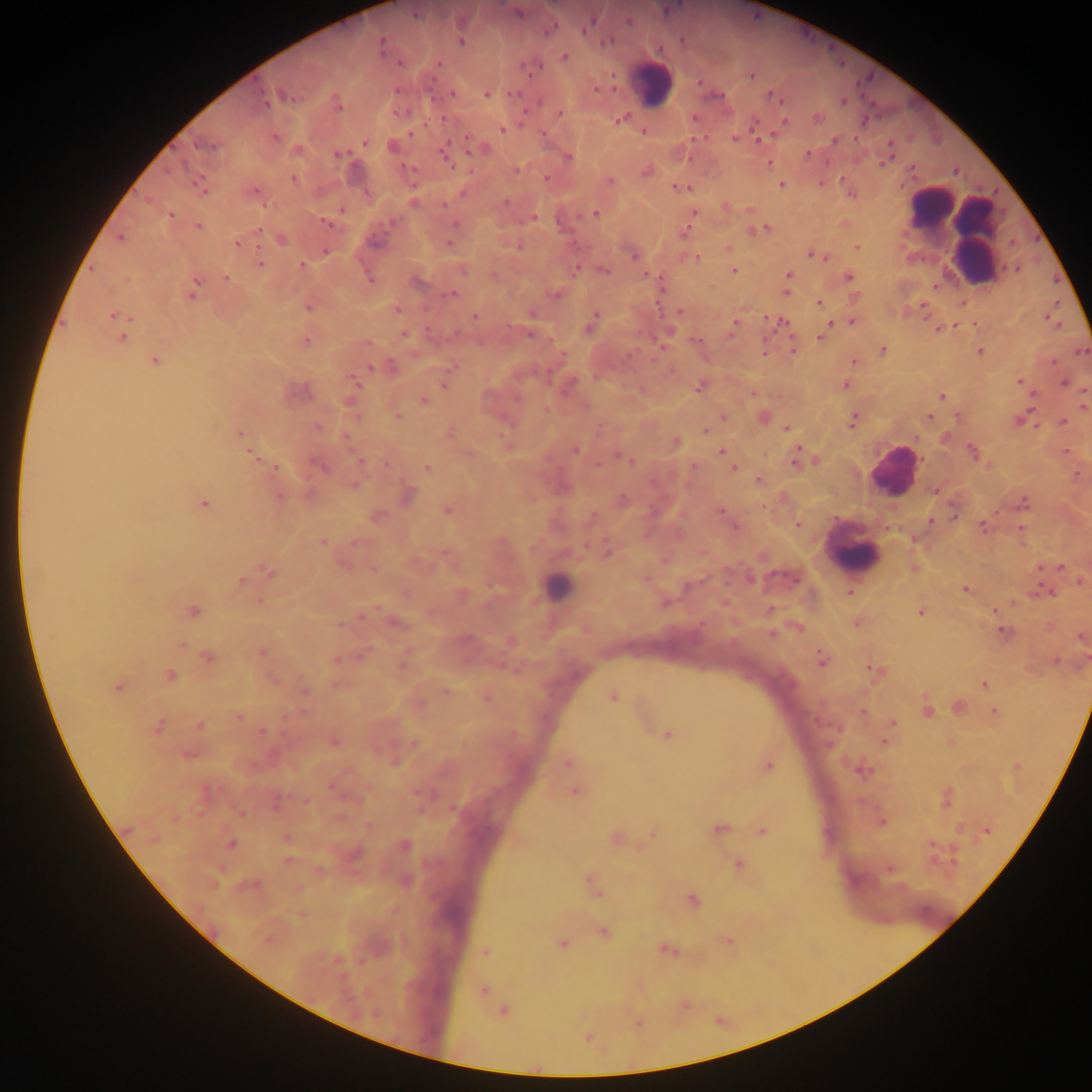 Approximate centers as [x, y] in pixels. Malaria parasite locations: [518, 13], [416, 15], [590, 23], [551, 29], [462, 41], [607, 42], [381, 45], [564, 56], [398, 62], [438, 64], [751, 76], [452, 94], [486, 95], [771, 96], [291, 97], [265, 101], [843, 102], [338, 105], [560, 114], [817, 117], [620, 119], [784, 122], [502, 129], [411, 133], [543, 134], [275, 137], [734, 137], [467, 138], [835, 141], [365, 142], [204, 146], [392, 146], [443, 151], [340, 155], [807, 155], [568, 157], [769, 163], [883, 163], [517, 170], [647, 171], [294, 178], [547, 178], [610, 181], [781, 185], [678, 187], [201, 188], [255, 191], [463, 193], [506, 202], [444, 205], [342, 210], [595, 213], [694, 213], [170, 215], [534, 218], [326, 223], [454, 224], [198, 226], [258, 229], [765, 229], [121, 239], [281, 239], [237, 244], [448, 244], [856, 246], [326, 251], [633, 256], [814, 256], [697, 258], [260, 263], [302, 265], [575, 269], [463, 270], [734, 271], [604, 272], [789, 274], [849, 278], [225, 279], [369, 279], [195, 285], [786, 292], [452, 294], [553, 294], [192, 295], [818, 303], [308, 307], [397, 309], [679, 312], [112, 315], [474, 315], [595, 315], [593, 321], [782, 322], [852, 322], [735, 324], [590, 328], [938, 328], [531, 334], [403, 335], [122, 337], [822, 337], [306, 342], [793, 349], [883, 351], [980, 352], [155, 362], [852, 362], [392, 367], [371, 368], [353, 380], [1019, 382], [1064, 383], [845, 385], [444, 386], [700, 387], [943, 396], [517, 398], [424, 402], [398, 416], [724, 416], [764, 417], [929, 417], [852, 420], [1063, 422], [318, 427], [787, 428], [705, 430], [239, 434], [347, 438], [676, 443], [575, 450], [722, 451], [974, 452], [618, 455], [254, 456], [624, 458], [796, 459], [360, 460], [598, 465], [693, 466], [320, 467], [276, 468], [427, 468], [733, 468], [1077, 474], [758, 479], [354, 485], [935, 491], [279, 497], [623, 501], [1024, 501], [203, 504], [447, 511], [719, 512], [377, 517], [797, 524], [983, 526], [736, 527], [323, 541], [355, 543], [608, 552], [1060, 567], [373, 569], [270, 573], [646, 580], [240, 582], [965, 589], [850, 592], [995, 611], [193, 612], [921, 612], [1004, 632], [772, 634], [1082, 637], [182, 645], [262, 653], [207, 657], [821, 659], [337, 660], [876, 670], [170, 676], [273, 681], [984, 684], [117, 688], [304, 688], [446, 692], [612, 697], [487, 698], [960, 708], [928, 711], [994, 711], [863, 712], [238, 717], [893, 722], [199, 725], [159, 726], [262, 732], [668, 735], [334, 742], [885, 742], [567, 763], [768, 766], [863, 772], [576, 791], [947, 798], [306, 801], [241, 814], [719, 830], [986, 830], [763, 831], [652, 833], [287, 838], [231, 844], [405, 846], [288, 861], [738, 865], [593, 885], [596, 892], [693, 900], [603, 932], [728, 941], [562, 943], [667, 951], [485, 952], [483, 990], [502, 1011]. Leukocyte locations: [654, 85], [929, 207], [967, 235], [893, 471], [852, 553], [557, 585]. Mobile-phone photograph taken through the microscope. Collected in Ghana. Thick blood smear. Single field of view. Image is 1092×1092 pixels.